Identify the parasite.
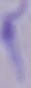
This is a trypanosome.

Captured at 1000x magnification. Micrograph.